Assess the morphology of the erythrocytes.
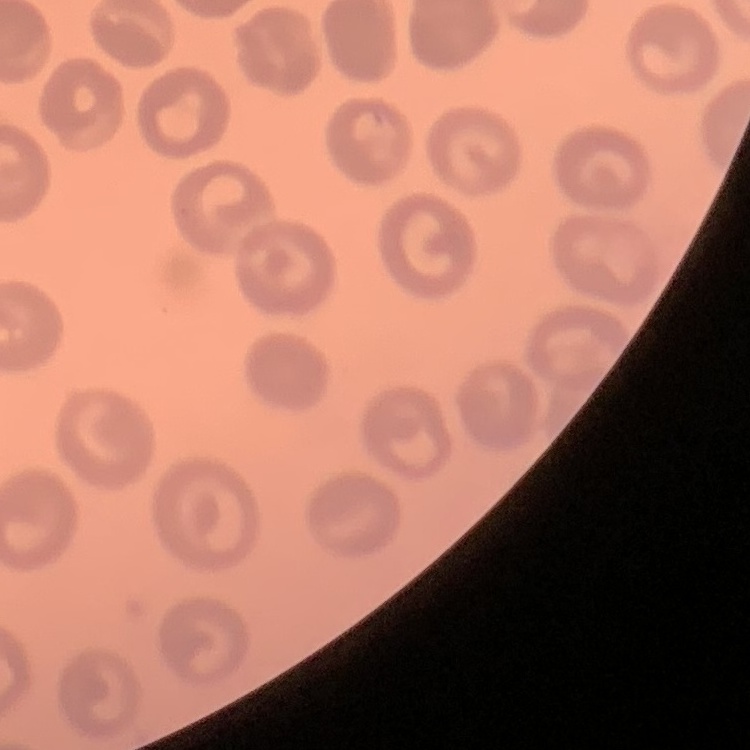
No rouleaux formation.

Thin peripheral smear. Square crop of a larger photomicrograph. Stained with either Field's or Giemsa.